Outline platelets.
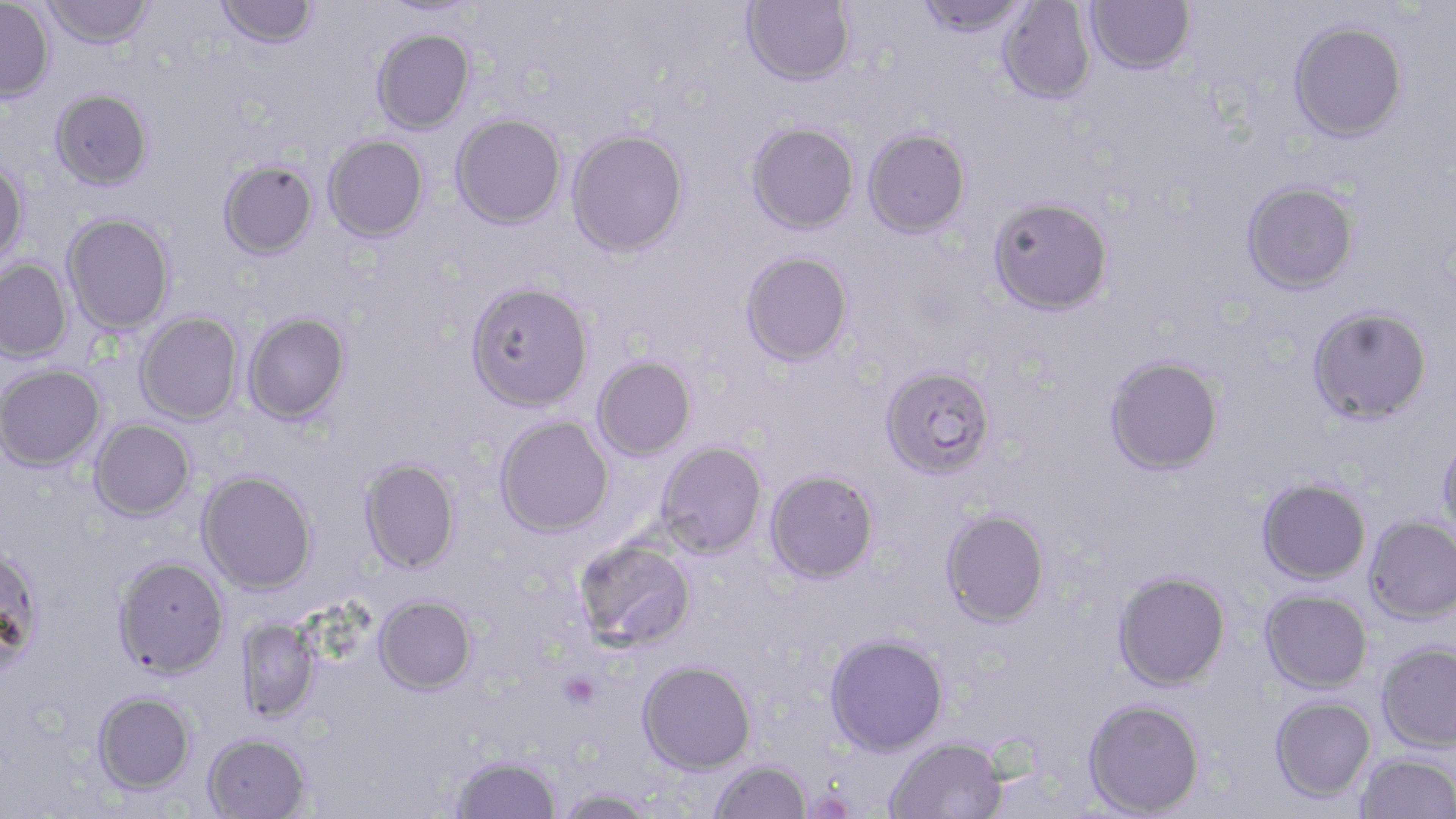

Approximate bounding boxes as named x1/y1/x2/y2 corners in pixels.
Platelets: (x1=561, y1=672, x2=600, y2=709).

Summary:
  - Uninfected red blood cell locations: (x1=43, y1=0, x2=153, y2=48), (x1=742, y1=0, x2=855, y2=85), (x1=915, y1=0, x2=1032, y2=37), (x1=1085, y1=0, x2=1195, y2=74), (x1=0, y1=1, x2=54, y2=103), (x1=215, y1=1, x2=319, y2=49), (x1=377, y1=1, x2=480, y2=18), (x1=997, y1=1, x2=1097, y2=104), (x1=1288, y1=20, x2=1408, y2=142), (x1=372, y1=28, x2=475, y2=135), (x1=50, y1=88, x2=153, y2=190), (x1=451, y1=113, x2=566, y2=229), (x1=746, y1=121, x2=859, y2=233), (x1=567, y1=128, x2=689, y2=256), (x1=863, y1=128, x2=971, y2=237), (x1=323, y1=134, x2=429, y2=242), (x1=218, y1=159, x2=318, y2=259), (x1=0, y1=160, x2=28, y2=269), (x1=1241, y1=180, x2=1359, y2=295), (x1=988, y1=196, x2=1114, y2=315), (x1=62, y1=212, x2=175, y2=335), (x1=740, y1=251, x2=853, y2=366), (x1=0, y1=258, x2=73, y2=363), (x1=466, y1=281, x2=594, y2=412), (x1=1307, y1=305, x2=1433, y2=424), (x1=135, y1=312, x2=243, y2=425), (x1=242, y1=312, x2=351, y2=425), (x1=1104, y1=355, x2=1224, y2=475), (x1=592, y1=356, x2=696, y2=461), (x1=0, y1=364, x2=106, y2=471), (x1=881, y1=365, x2=997, y2=479), (x1=495, y1=416, x2=614, y2=537), (x1=89, y1=419, x2=196, y2=521), (x1=1438, y1=434, x2=1456, y2=539), (x1=656, y1=441, x2=767, y2=558), (x1=359, y1=457, x2=462, y2=574), (x1=765, y1=469, x2=880, y2=583), (x1=197, y1=471, x2=317, y2=594), (x1=1257, y1=478, x2=1371, y2=585), (x1=941, y1=508, x2=1050, y2=628), (x1=1365, y1=516, x2=1456, y2=624), (x1=572, y1=535, x2=697, y2=652), (x1=0, y1=543, x2=46, y2=675), (x1=113, y1=555, x2=230, y2=678), (x1=1113, y1=571, x2=1232, y2=691), (x1=1260, y1=589, x2=1372, y2=693), (x1=374, y1=594, x2=477, y2=695), (x1=238, y1=618, x2=320, y2=723), (x1=824, y1=634, x2=948, y2=756), (x1=1377, y1=642, x2=1456, y2=753), (x1=637, y1=659, x2=757, y2=774), (x1=92, y1=690, x2=197, y2=795), (x1=1270, y1=695, x2=1376, y2=802), (x1=1083, y1=698, x2=1205, y2=817), (x1=202, y1=732, x2=312, y2=819), (x1=885, y1=737, x2=1007, y2=819), (x1=1356, y1=752, x2=1456, y2=819), (x1=450, y1=754, x2=561, y2=818), (x1=708, y1=759, x2=812, y2=819), (x1=553, y1=787, x2=658, y2=818)
  - Slide-level diagnosis: Plasmodium falciparum
  - Magnification: 1000x
  - Stain: May-Grünwald-Giemsa
  - Field of view: one of a larger specimen
  - Modality: light microscopy
  - Image size: 1456×819 pixels
  - Preparation: thin blood film